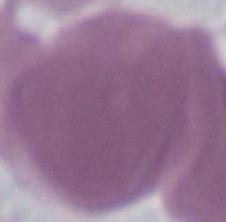

Summary:
  - Modality: micrograph
  - Magnification: 1000x
  - Identification: erythrocyte